Point out Plasmodium parasites and leukocytes.
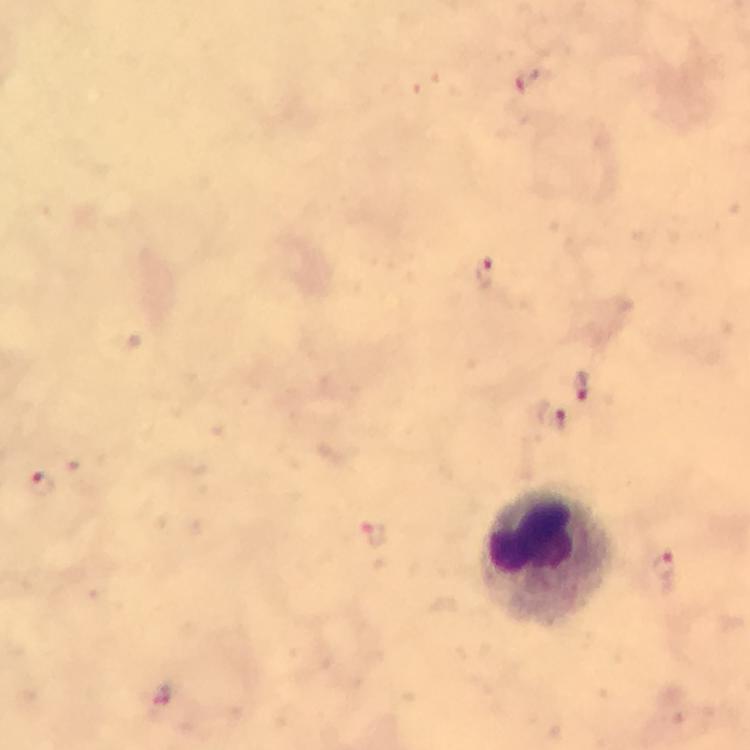
Approximate centers as [x, y] in pixels.
Plasmodium parasites: [530, 79], [485, 273], [582, 388], [551, 415], [41, 482], [371, 534], [663, 571], [162, 696].
Leukocytes: [545, 559].

Summary:
  - Stain: Giemsa
  - Capture: smartphone camera through the microscope
  - Image size: 750×750 pixels
  - Cropped from: one field of view
  - Preparation: thick smear
  - Immersion oil: applied
  - Magnification: 100x
  - Context: from a malaria diagnostic workup